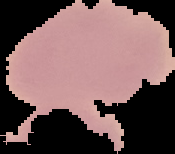 Image is 175×154 pixels. From a thin blood film. Cell region segmented out of the field of view; the surrounding area is masked to black. Result: no Plasmodium parasites detected.